Classify this cell by malaria status.
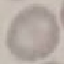
Uninfected.

Summary:
  - Image type: automatically extracted cell patch, resized to 64 × 64 pixels
  - Preparation: thin blood smear
  - Stain: Giemsa
  - Capture: smartphone through the microscope eyepiece